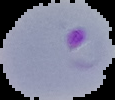
Malaria status: parasitized. Image is 115×100 pixels. From a thin blood smear. The area outside the segmented cell region is set to black.